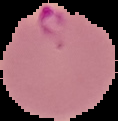
Summary:
  - Preparation: thin blood smear
  - Image size: 118×121 pixels
  - Malaria status: parasitized
  - Image type: cell region segmented out of the field of view; surrounding area masked to black